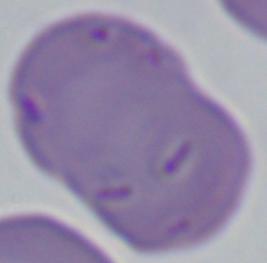
Summary:
  - Identification: Babesia
  - Modality: photomicrograph
  - Magnification: 1000x